Identify the parasite.
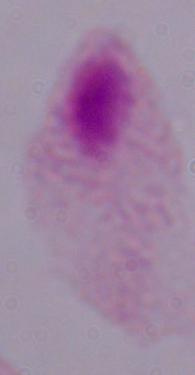
A trichomonad.

Photomicrograph. Captured at 1000x magnification.